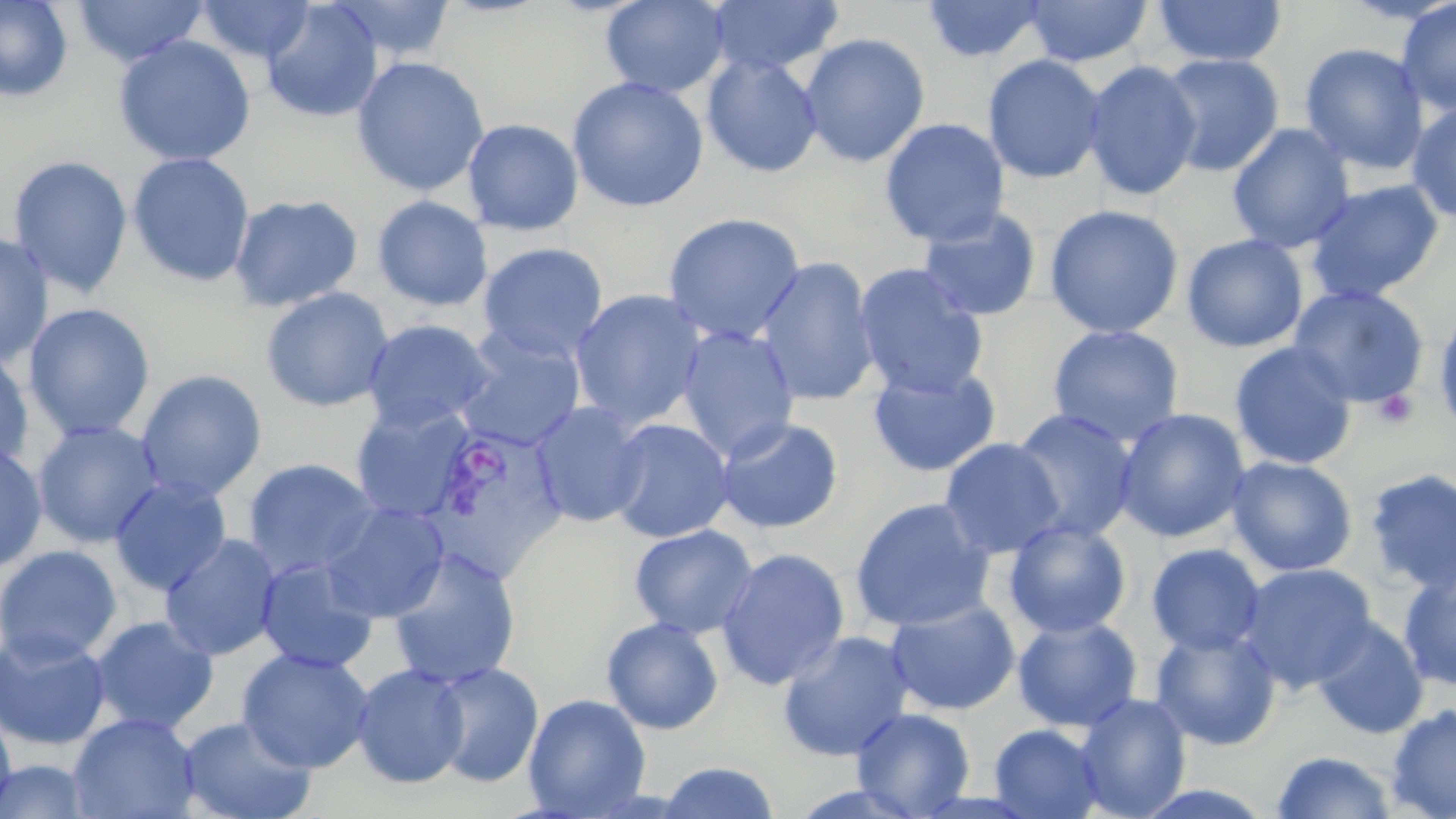

Summary:
  - Coordinate format: approximate bounding boxes as (x1, y1, x2, y2) in pixels
  - Platelet locations: (1372, 388, 1418, 429)
  - Uninfected red blood cell locations: (71, 0, 209, 66), (197, 0, 316, 64), (325, 0, 456, 62), (600, 0, 730, 97), (707, 0, 844, 76), (920, 0, 1049, 64), (1024, 0, 1153, 67), (1152, 0, 1287, 67), (1341, 0, 1454, 25), (1395, 0, 1456, 117), (0, 1, 73, 101), (261, 2, 383, 122), (799, 32, 930, 168), (113, 35, 256, 167), (1299, 42, 1429, 175), (701, 53, 823, 179), (982, 54, 1106, 185), (1157, 54, 1284, 177), (351, 55, 490, 197), (1082, 61, 1202, 202), (567, 75, 708, 213), (1406, 102, 1456, 224), (879, 117, 1010, 247), (462, 118, 584, 236), (1227, 123, 1355, 253), (126, 152, 255, 287), (7, 155, 133, 298), (1304, 179, 1445, 304), (228, 194, 363, 312), (372, 195, 493, 311), (1043, 204, 1184, 339), (916, 207, 1042, 322), (662, 212, 807, 346), (0, 232, 55, 367), (1182, 234, 1309, 353), (477, 243, 609, 364), (754, 256, 881, 406), (852, 262, 989, 398), (1288, 285, 1430, 408), (260, 287, 394, 412), (568, 289, 708, 429), (23, 302, 157, 441), (1433, 304, 1456, 439), (362, 319, 499, 434), (1047, 324, 1185, 447), (676, 326, 801, 461), (453, 333, 586, 453), (1229, 342, 1358, 471), (0, 348, 35, 474), (867, 364, 1001, 478), (135, 369, 267, 502), (529, 401, 650, 528), (348, 404, 477, 523), (1114, 407, 1251, 544), (1010, 408, 1139, 543), (714, 416, 844, 534), (606, 417, 735, 543), (32, 420, 164, 549), (939, 438, 1066, 559), (0, 442, 48, 573), (1226, 456, 1358, 577), (243, 457, 381, 579), (1363, 468, 1456, 595), (108, 476, 233, 596), (849, 498, 996, 632), (319, 502, 450, 622), (1003, 519, 1131, 639), (629, 524, 758, 638), (159, 533, 283, 662), (1146, 543, 1266, 656), (0, 545, 122, 666), (715, 546, 851, 691), (386, 547, 523, 689), (255, 557, 381, 674), (1237, 562, 1378, 694), (1398, 568, 1456, 691), (884, 597, 1021, 716), (89, 615, 219, 735), (1012, 616, 1143, 733), (1311, 617, 1429, 739), (600, 618, 724, 735), (1149, 626, 1281, 750), (0, 628, 112, 751), (776, 630, 915, 762), (237, 647, 375, 774), (428, 660, 545, 787), (352, 663, 469, 790), (1074, 693, 1192, 819), (522, 694, 651, 817), (1386, 703, 1456, 819), (0, 707, 16, 815), (850, 707, 975, 818), (67, 712, 200, 819), (177, 715, 317, 819), (989, 723, 1106, 819), (1270, 750, 1400, 819), (0, 760, 97, 818), (655, 761, 782, 818)
  - Plasmodium vivax-infected red blood cell locations: (430, 434, 568, 580)
  - Slide-level diagnosis: Plasmodium vivax
  - Image size: 1456×819 pixels
  - Stain: May-Grünwald-Giemsa
  - Modality: optical microscopy
  - Preparation: thin blood smear
  - Field of view: single
  - Magnification: 1000x